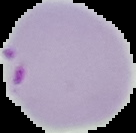

image type = cell region segmented out of the field of view; surrounding area masked to black
preparation = thin blood smear
result = malaria parasites detected
image size = 136×133 pixels